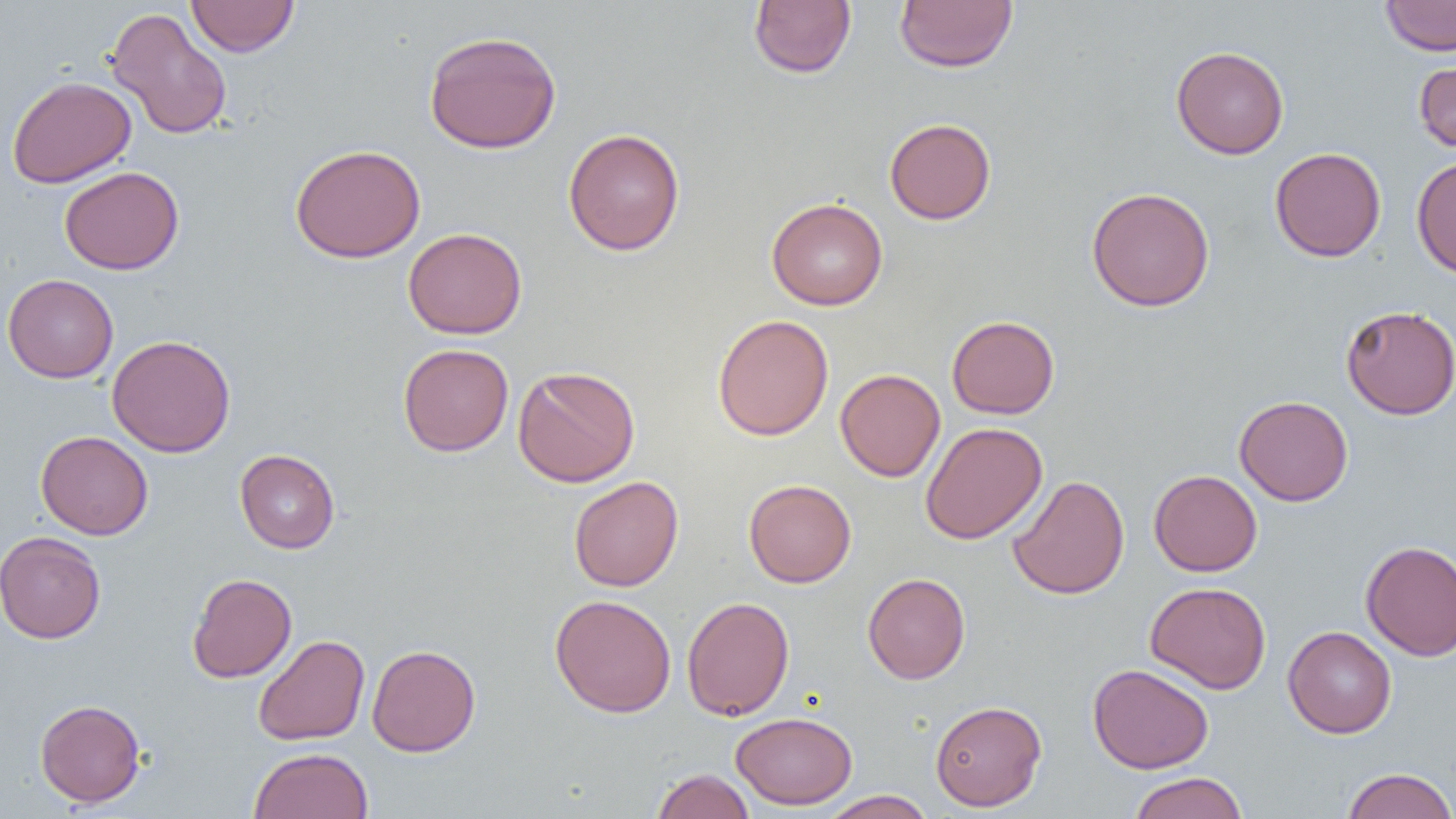
Summary:
  - Coordinate format: approximate bounding boxes as named x1/y1/x2/y2 corners in pixels
  - Uninfected red blood cell locations: (x1=186, y1=0, x2=299, y2=57), (x1=748, y1=0, x2=857, y2=78), (x1=894, y1=0, x2=1018, y2=73), (x1=1380, y1=0, x2=1456, y2=56), (x1=105, y1=7, x2=233, y2=141), (x1=424, y1=30, x2=562, y2=154), (x1=1170, y1=45, x2=1289, y2=159), (x1=1414, y1=60, x2=1456, y2=154), (x1=7, y1=75, x2=136, y2=188), (x1=884, y1=118, x2=996, y2=224), (x1=562, y1=128, x2=686, y2=255), (x1=290, y1=143, x2=426, y2=263), (x1=1269, y1=147, x2=1386, y2=262), (x1=1411, y1=155, x2=1456, y2=278), (x1=59, y1=166, x2=184, y2=275), (x1=1086, y1=186, x2=1215, y2=311), (x1=766, y1=197, x2=888, y2=310), (x1=403, y1=227, x2=527, y2=339), (x1=3, y1=273, x2=119, y2=383), (x1=1341, y1=304, x2=1456, y2=419), (x1=712, y1=314, x2=834, y2=441), (x1=947, y1=315, x2=1060, y2=419), (x1=106, y1=334, x2=236, y2=457), (x1=398, y1=343, x2=514, y2=456), (x1=513, y1=365, x2=640, y2=488), (x1=835, y1=368, x2=945, y2=482), (x1=1234, y1=395, x2=1353, y2=506), (x1=920, y1=422, x2=1047, y2=544), (x1=35, y1=430, x2=153, y2=540), (x1=235, y1=449, x2=340, y2=553), (x1=1149, y1=469, x2=1262, y2=576), (x1=1007, y1=474, x2=1130, y2=600), (x1=569, y1=476, x2=684, y2=592), (x1=744, y1=478, x2=856, y2=588), (x1=1, y1=531, x2=106, y2=644), (x1=1361, y1=540, x2=1456, y2=661), (x1=862, y1=572, x2=970, y2=684), (x1=187, y1=573, x2=297, y2=682), (x1=1145, y1=581, x2=1271, y2=694), (x1=549, y1=594, x2=677, y2=718), (x1=681, y1=595, x2=795, y2=721), (x1=1283, y1=626, x2=1397, y2=738), (x1=253, y1=634, x2=370, y2=745), (x1=366, y1=644, x2=481, y2=756), (x1=1087, y1=663, x2=1214, y2=773), (x1=34, y1=698, x2=146, y2=807), (x1=930, y1=699, x2=1047, y2=811), (x1=730, y1=711, x2=858, y2=810), (x1=249, y1=748, x2=374, y2=819), (x1=1341, y1=767, x2=1456, y2=819), (x1=651, y1=768, x2=756, y2=819), (x1=1128, y1=772, x2=1248, y2=819), (x1=820, y1=790, x2=936, y2=819)
  - Slide-level diagnosis: negative for blood parasites
  - Field of view: one of a larger specimen
  - Image size: 1456×819 pixels
  - Magnification: 1000x
  - Modality: light microscopy
  - Preparation: thin blood smear